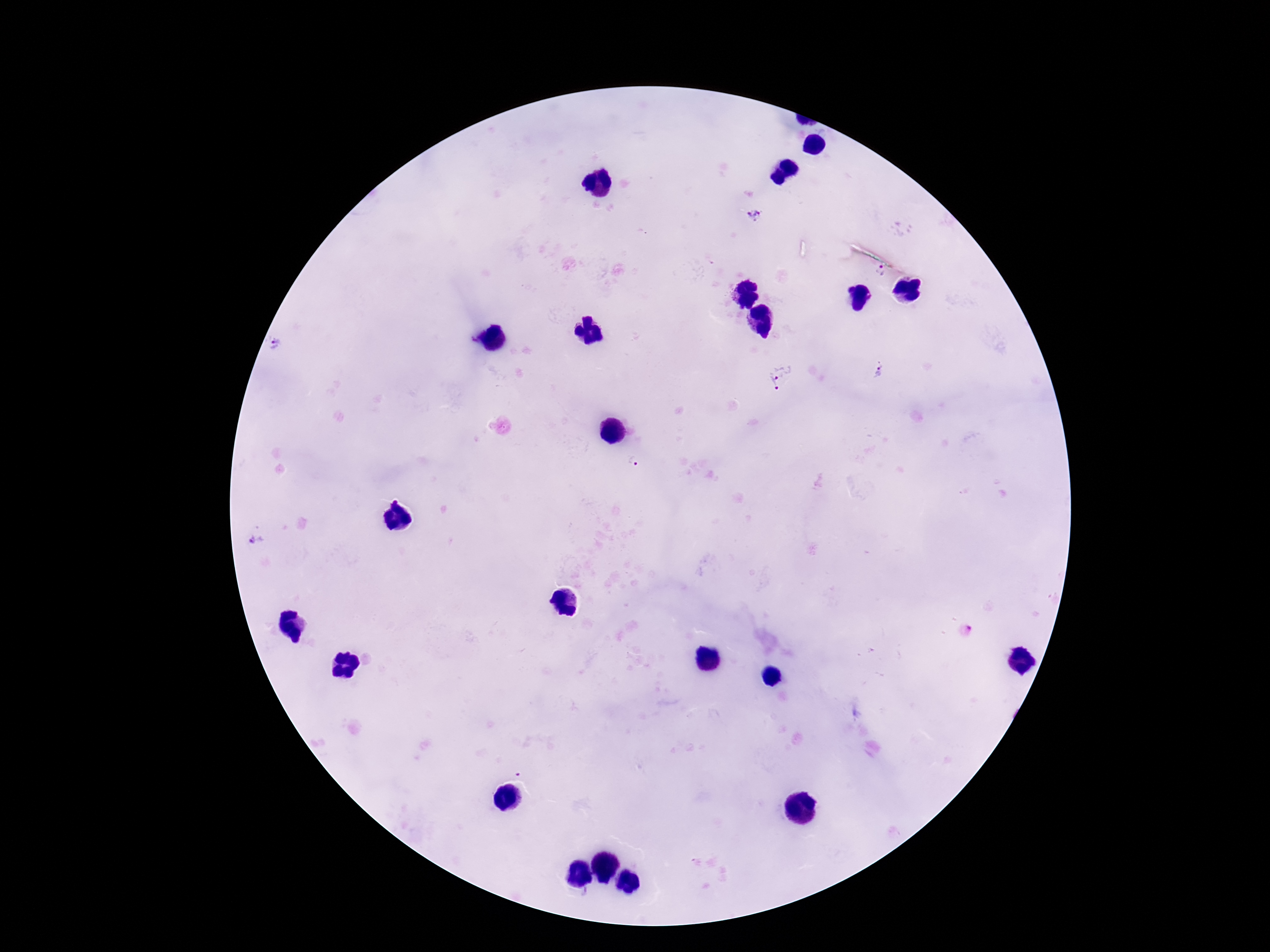

{
  "plasmodium_parasite_locations": "approximate centers as {x, y} in pixels: {754, 215}, {883, 269}, {277, 345}, {881, 371}, {781, 377}, {632, 463}, {259, 536}",
  "preparation": "thick peripheral-blood smear",
  "magnification": "100x",
  "field_of_view": "one from this slide",
  "capture": "smartphone camera through the microscope eyepiece",
  "image_size": "1270×952 pixels",
  "patient_malaria_status": "infected",
  "stain": "Giemsa"
}